Classify this cell by malaria status.
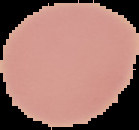
It is uninfected.

Summary:
  - Preparation: thin blood film
  - Image size: 139×130 pixels
  - Image type: segmented cell region with the area outside set to black